Locate every blood parasite and identify its species.
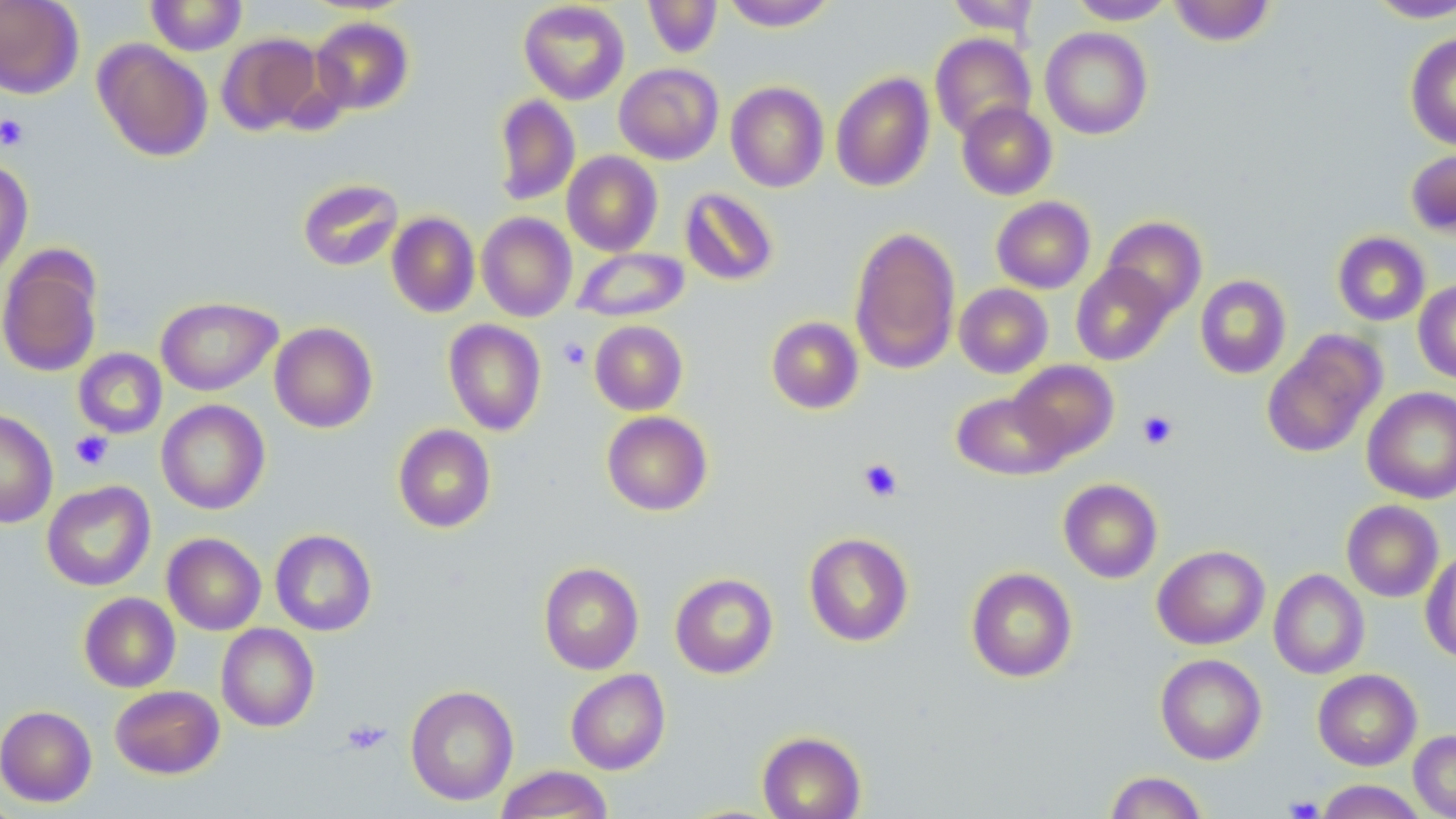

No blood parasites observed.

Approximate bounding boxes as named x1/y1/x2/y2 corners in pixels. Uninfected red blood cell locations: (x1=0, y1=0, x2=84, y2=99), (x1=146, y1=0, x2=247, y2=56), (x1=643, y1=0, x2=722, y2=58), (x1=721, y1=0, x2=837, y2=31), (x1=945, y1=0, x2=1042, y2=36), (x1=1068, y1=0, x2=1176, y2=24), (x1=1365, y1=0, x2=1456, y2=23), (x1=518, y1=1, x2=630, y2=104), (x1=1169, y1=1, x2=1275, y2=46), (x1=310, y1=16, x2=414, y2=115), (x1=1039, y1=27, x2=1153, y2=139), (x1=217, y1=32, x2=324, y2=135), (x1=930, y1=33, x2=1036, y2=141), (x1=1405, y1=33, x2=1456, y2=151), (x1=93, y1=39, x2=213, y2=162), (x1=614, y1=63, x2=724, y2=164), (x1=830, y1=71, x2=935, y2=192), (x1=726, y1=81, x2=829, y2=192), (x1=494, y1=95, x2=580, y2=206), (x1=956, y1=100, x2=1057, y2=200), (x1=1405, y1=148, x2=1456, y2=237), (x1=562, y1=151, x2=663, y2=256), (x1=0, y1=159, x2=33, y2=282), (x1=298, y1=178, x2=403, y2=271), (x1=679, y1=187, x2=780, y2=287), (x1=991, y1=196, x2=1095, y2=293), (x1=387, y1=212, x2=480, y2=317), (x1=476, y1=213, x2=577, y2=322), (x1=1101, y1=215, x2=1206, y2=318), (x1=848, y1=225, x2=961, y2=374), (x1=1333, y1=231, x2=1430, y2=326), (x1=0, y1=246, x2=104, y2=378), (x1=571, y1=247, x2=690, y2=322), (x1=1071, y1=263, x2=1174, y2=365), (x1=1195, y1=275, x2=1291, y2=379), (x1=1413, y1=279, x2=1456, y2=383), (x1=955, y1=283, x2=1053, y2=378), (x1=156, y1=296, x2=281, y2=396), (x1=766, y1=316, x2=864, y2=414), (x1=443, y1=319, x2=547, y2=435), (x1=589, y1=320, x2=688, y2=415), (x1=269, y1=322, x2=378, y2=433), (x1=1262, y1=332, x2=1383, y2=458), (x1=73, y1=348, x2=167, y2=439), (x1=1008, y1=360, x2=1119, y2=461), (x1=1362, y1=387, x2=1456, y2=503), (x1=951, y1=391, x2=1069, y2=481), (x1=156, y1=399, x2=270, y2=515), (x1=0, y1=409, x2=58, y2=528), (x1=602, y1=410, x2=712, y2=516), (x1=393, y1=424, x2=496, y2=533), (x1=1058, y1=478, x2=1163, y2=583), (x1=42, y1=480, x2=156, y2=592), (x1=1341, y1=500, x2=1444, y2=602), (x1=270, y1=529, x2=377, y2=636), (x1=803, y1=532, x2=914, y2=646), (x1=163, y1=533, x2=266, y2=635), (x1=1153, y1=545, x2=1269, y2=649), (x1=1421, y1=549, x2=1456, y2=663), (x1=538, y1=561, x2=644, y2=674), (x1=966, y1=567, x2=1078, y2=682), (x1=1269, y1=569, x2=1369, y2=679), (x1=670, y1=572, x2=779, y2=678), (x1=79, y1=592, x2=180, y2=692), (x1=216, y1=623, x2=319, y2=732), (x1=1155, y1=653, x2=1267, y2=765), (x1=1313, y1=668, x2=1422, y2=771), (x1=566, y1=669, x2=671, y2=774), (x1=110, y1=685, x2=224, y2=779), (x1=405, y1=685, x2=519, y2=806), (x1=0, y1=705, x2=97, y2=807), (x1=757, y1=730, x2=866, y2=819), (x1=1409, y1=730, x2=1456, y2=819), (x1=494, y1=765, x2=614, y2=818), (x1=1104, y1=771, x2=1209, y2=819), (x1=1315, y1=780, x2=1428, y2=818). Platelet locations: (x1=0, y1=114, x2=30, y2=151), (x1=558, y1=337, x2=591, y2=370), (x1=1137, y1=410, x2=1178, y2=449), (x1=70, y1=431, x2=113, y2=470), (x1=858, y1=458, x2=903, y2=502), (x1=341, y1=718, x2=391, y2=755), (x1=1284, y1=795, x2=1324, y2=819). Slide-level diagnosis: no evidence of blood parasites. 1000x magnification. Light microscopy. Image is 1456×819 pixels. One field of a larger specimen. May-Grünwald-Giemsa-stained preparation. Thin blood smear.